Outline each blood parasite and name the species.
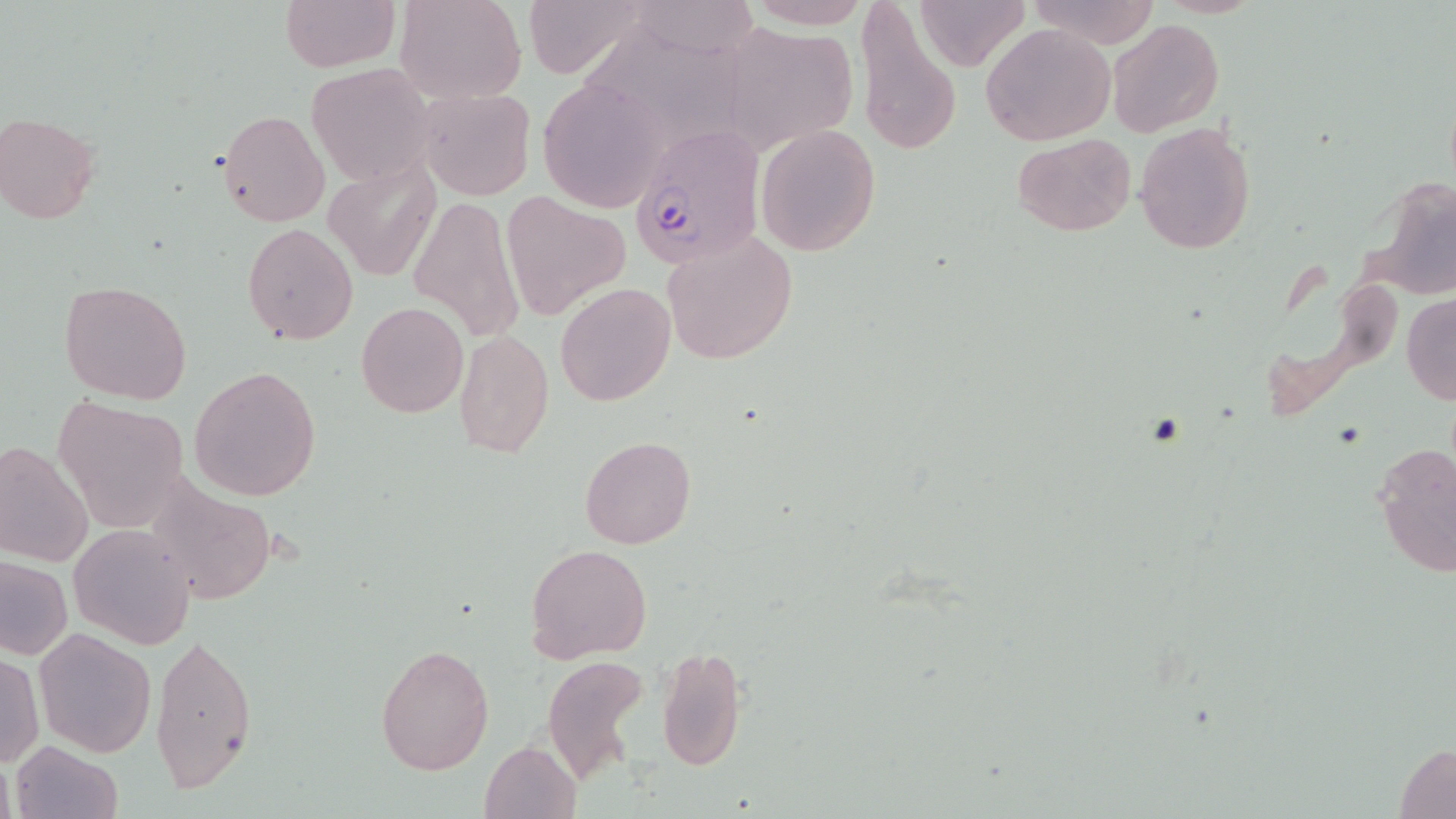

Approximate bounding boxes as [x1, y1, x2, y2] in pixels.
Plasmodium falciparum-infected red blood cells: [632, 123, 766, 267].
No Plasmodium ovale, Plasmodium malariae, Plasmodium vivax, Babesia divergens, or Trypanosoma brucei observed.

Summary:
  - Uninfected red blood cell locations: [280, 0, 398, 72], [397, 0, 526, 103], [522, 0, 648, 79], [913, 0, 1027, 69], [1028, 0, 1162, 48], [744, 1, 877, 29], [622, 2, 763, 60], [855, 4, 962, 157], [1106, 18, 1223, 138], [719, 22, 860, 155], [979, 23, 1116, 147], [593, 29, 749, 151], [306, 61, 438, 186], [539, 77, 668, 209], [417, 86, 535, 202], [1, 110, 101, 224], [217, 110, 330, 228], [1134, 120, 1257, 254], [755, 123, 881, 257], [1014, 134, 1133, 237], [327, 161, 440, 283], [1373, 175, 1456, 299], [503, 192, 629, 321], [409, 194, 524, 346], [242, 223, 359, 346], [661, 229, 797, 366], [58, 280, 191, 405], [555, 282, 675, 406], [1402, 295, 1456, 404], [356, 301, 469, 418], [453, 327, 553, 460], [189, 366, 322, 503], [51, 395, 189, 531], [579, 436, 697, 550], [0, 440, 96, 567], [1371, 441, 1456, 580], [140, 479, 278, 606], [67, 522, 195, 650], [524, 544, 653, 665], [0, 556, 72, 660], [34, 628, 158, 756], [150, 629, 256, 796], [373, 642, 494, 776], [657, 645, 748, 771], [1, 653, 42, 767], [540, 655, 652, 785], [479, 740, 581, 818], [1393, 741, 1456, 818], [10, 742, 123, 819]
  - Slide-level diagnosis: Plasmodium falciparum
  - Stain: May-Grünwald-Giemsa
  - Image size: 1456×819 pixels
  - Preparation: thin blood film
  - Field of view: one of a larger specimen
  - Modality: optical microscopy
  - Magnification: 1000x